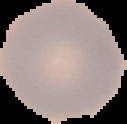

Summary:
  - Image size: 127×124 pixels
  - Preparation: thin blood smear
  - Image type: segmented cell region on a black background
  - Result: negative for malaria parasites